Give the extent of all white blood cells.
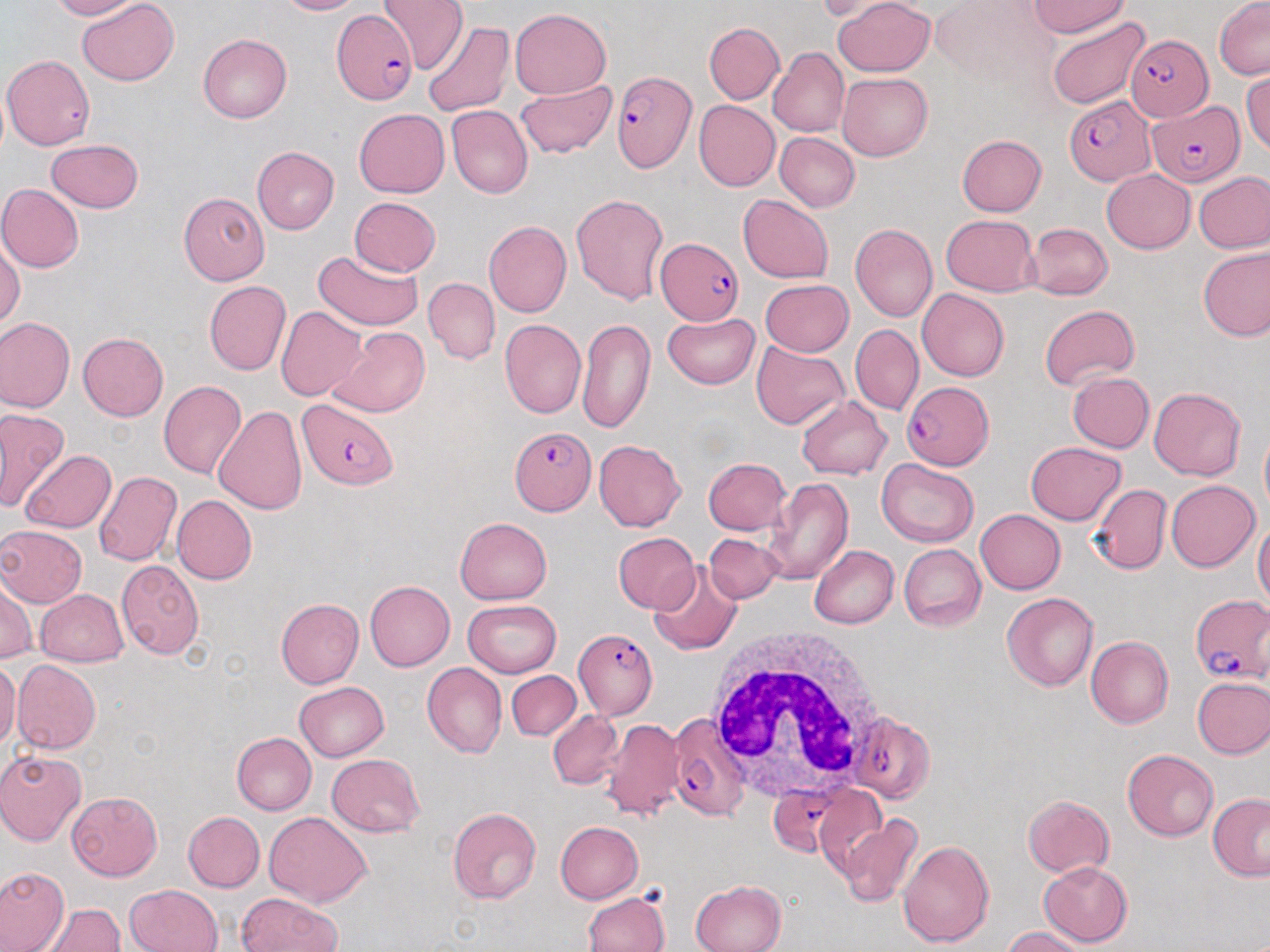

Approximate bounding boxes as named x1/y1/x2/y2 corners in pixels.
White blood cells: (x1=704, y1=628, x2=894, y2=804).

{
  "slide_level_diagnosis": "Plasmodium falciparum",
  "preparation": "thin blood film",
  "plasmodium_falciparum_infected_red_blood_cell_locations": "approximate bounding boxes as named x1/y1/x2/y2 corners in pixels: (x1=332, y1=8, x2=417, y2=104), (x1=1125, y1=34, x2=1213, y2=121), (x1=613, y1=70, x2=697, y2=172), (x1=1065, y1=95, x2=1156, y2=184), (x1=1147, y1=102, x2=1246, y2=186), (x1=655, y1=237, x2=744, y2=327), (x1=902, y1=382, x2=993, y2=468), (x1=297, y1=398, x2=397, y2=489), (x1=510, y1=426, x2=596, y2=515), (x1=1191, y1=593, x2=1270, y2=683), (x1=573, y1=629, x2=657, y2=719), (x1=846, y1=712, x2=936, y2=804), (x1=666, y1=715, x2=751, y2=820), (x1=767, y1=787, x2=841, y2=859)",
  "magnification": "1000x",
  "uninfected_red_blood_cell_locations": "approximate bounding boxes as named x1/y1/x2/y2 corners in pixels: (x1=47, y1=0, x2=141, y2=19), (x1=77, y1=0, x2=178, y2=86), (x1=274, y1=0, x2=364, y2=15), (x1=378, y1=0, x2=467, y2=73), (x1=832, y1=0, x2=935, y2=77), (x1=929, y1=0, x2=1055, y2=85), (x1=1030, y1=0, x2=1131, y2=38), (x1=1214, y1=0, x2=1270, y2=80), (x1=814, y1=1, x2=905, y2=24), (x1=510, y1=8, x2=611, y2=99), (x1=1048, y1=17, x2=1151, y2=110), (x1=422, y1=20, x2=516, y2=119), (x1=704, y1=22, x2=784, y2=103), (x1=197, y1=33, x2=291, y2=123), (x1=768, y1=48, x2=849, y2=138), (x1=2, y1=54, x2=96, y2=150), (x1=1243, y1=72, x2=1270, y2=156), (x1=837, y1=73, x2=932, y2=160), (x1=515, y1=79, x2=616, y2=158), (x1=694, y1=101, x2=780, y2=191), (x1=446, y1=105, x2=532, y2=198), (x1=353, y1=108, x2=449, y2=198), (x1=774, y1=132, x2=860, y2=211), (x1=957, y1=135, x2=1046, y2=216), (x1=46, y1=138, x2=144, y2=213), (x1=252, y1=147, x2=339, y2=233), (x1=1102, y1=170, x2=1195, y2=253), (x1=1194, y1=171, x2=1270, y2=253), (x1=0, y1=184, x2=85, y2=273), (x1=178, y1=192, x2=269, y2=285), (x1=571, y1=192, x2=670, y2=305), (x1=738, y1=194, x2=833, y2=283), (x1=349, y1=197, x2=441, y2=276), (x1=942, y1=215, x2=1039, y2=295), (x1=484, y1=220, x2=571, y2=318), (x1=1026, y1=223, x2=1113, y2=299), (x1=849, y1=224, x2=937, y2=322), (x1=0, y1=237, x2=25, y2=330), (x1=1197, y1=246, x2=1269, y2=343), (x1=312, y1=250, x2=425, y2=331), (x1=424, y1=277, x2=500, y2=365), (x1=760, y1=279, x2=853, y2=356), (x1=204, y1=281, x2=291, y2=375), (x1=917, y1=289, x2=1009, y2=381), (x1=1040, y1=304, x2=1140, y2=389), (x1=277, y1=306, x2=367, y2=400), (x1=663, y1=311, x2=760, y2=388), (x1=0, y1=316, x2=75, y2=414), (x1=577, y1=318, x2=655, y2=434), (x1=500, y1=319, x2=586, y2=418), (x1=850, y1=324, x2=924, y2=416), (x1=327, y1=326, x2=428, y2=418), (x1=77, y1=333, x2=169, y2=421), (x1=751, y1=341, x2=849, y2=430), (x1=1065, y1=370, x2=1155, y2=451), (x1=159, y1=381, x2=245, y2=479), (x1=1150, y1=387, x2=1247, y2=480), (x1=797, y1=396, x2=891, y2=480), (x1=214, y1=404, x2=307, y2=513), (x1=0, y1=406, x2=68, y2=511), (x1=1260, y1=431, x2=1270, y2=517), (x1=594, y1=440, x2=686, y2=531), (x1=1025, y1=441, x2=1126, y2=525), (x1=20, y1=450, x2=116, y2=533), (x1=703, y1=457, x2=791, y2=535), (x1=878, y1=458, x2=979, y2=547), (x1=93, y1=471, x2=181, y2=566), (x1=762, y1=477, x2=852, y2=586), (x1=1167, y1=480, x2=1259, y2=571), (x1=1089, y1=483, x2=1171, y2=574), (x1=171, y1=494, x2=257, y2=584), (x1=975, y1=509, x2=1066, y2=593), (x1=455, y1=517, x2=551, y2=604), (x1=1253, y1=518, x2=1270, y2=607), (x1=0, y1=525, x2=87, y2=607), (x1=613, y1=533, x2=700, y2=612), (x1=704, y1=533, x2=781, y2=602), (x1=899, y1=544, x2=986, y2=631), (x1=810, y1=546, x2=898, y2=628), (x1=116, y1=559, x2=204, y2=659), (x1=649, y1=564, x2=743, y2=655), (x1=1, y1=578, x2=36, y2=663), (x1=364, y1=581, x2=454, y2=671), (x1=35, y1=589, x2=129, y2=668), (x1=1002, y1=592, x2=1099, y2=691), (x1=276, y1=598, x2=364, y2=689), (x1=462, y1=599, x2=561, y2=678), (x1=1085, y1=636, x2=1174, y2=728), (x1=0, y1=660, x2=20, y2=750), (x1=12, y1=660, x2=102, y2=753), (x1=423, y1=662, x2=506, y2=758), (x1=506, y1=671, x2=580, y2=740), (x1=1192, y1=677, x2=1270, y2=758), (x1=294, y1=681, x2=390, y2=761), (x1=548, y1=710, x2=624, y2=789), (x1=599, y1=719, x2=686, y2=821), (x1=232, y1=732, x2=316, y2=815), (x1=0, y1=749, x2=86, y2=845), (x1=1122, y1=750, x2=1219, y2=841), (x1=327, y1=754, x2=424, y2=836), (x1=813, y1=785, x2=887, y2=877), (x1=67, y1=792, x2=162, y2=880), (x1=1209, y1=793, x2=1270, y2=881), (x1=1022, y1=794, x2=1114, y2=878), (x1=447, y1=807, x2=541, y2=904), (x1=183, y1=812, x2=265, y2=892), (x1=264, y1=812, x2=372, y2=906), (x1=836, y1=814, x2=923, y2=908), (x1=555, y1=821, x2=643, y2=904), (x1=897, y1=840, x2=994, y2=948), (x1=1038, y1=861, x2=1133, y2=947), (x1=0, y1=866, x2=70, y2=952), (x1=690, y1=880, x2=787, y2=952), (x1=126, y1=884, x2=222, y2=952), (x1=583, y1=892, x2=670, y2=952), (x1=236, y1=893, x2=341, y2=951), (x1=41, y1=904, x2=125, y2=952), (x1=1001, y1=926, x2=1089, y2=951)",
  "stain": "May-Grünwald-Giemsa",
  "field_of_view": "single",
  "modality": "light microscopy",
  "image_size": "1270×952 pixels"
}